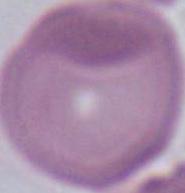 Photomicrograph. Captured at 1000x magnification. A red blood cell is seen.